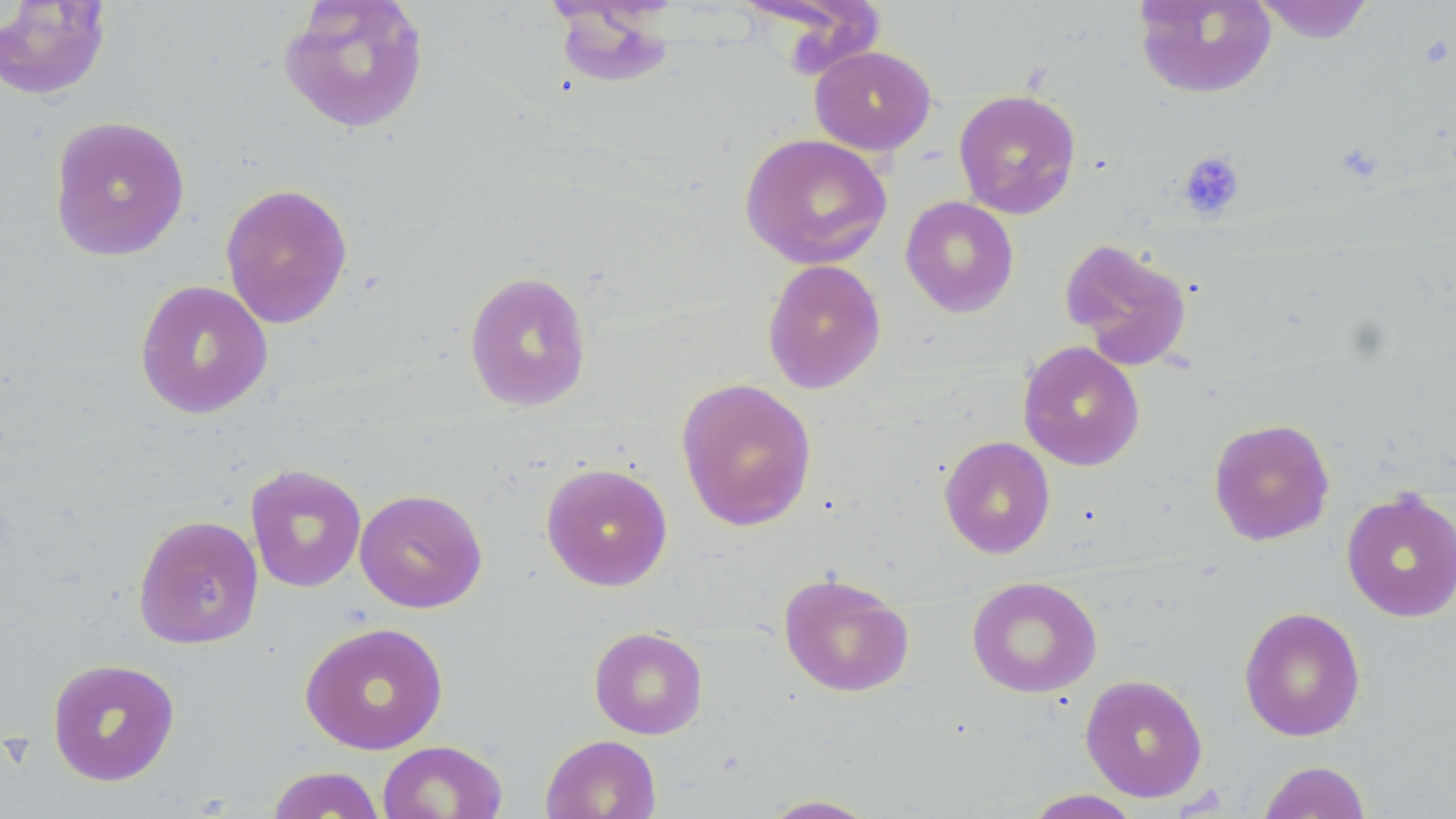

Approximate bounding boxes as (x1, y1, x2, y2) in pixels. Uninfected red blood cell locations: (277, 0, 430, 135), (1133, 0, 1277, 99), (1252, 0, 1376, 44), (0, 1, 112, 100), (549, 1, 676, 90), (810, 45, 937, 155), (953, 88, 1081, 219), (48, 115, 191, 262), (740, 133, 892, 270), (220, 182, 353, 329), (900, 196, 1020, 317), (1060, 238, 1194, 371), (762, 259, 887, 394), (463, 271, 592, 411), (134, 279, 273, 419), (1017, 341, 1145, 471), (675, 377, 817, 531), (1208, 417, 1335, 546), (939, 435, 1056, 558), (540, 462, 673, 591), (244, 463, 367, 593), (354, 488, 488, 614), (1340, 488, 1456, 623), (132, 513, 264, 650), (778, 571, 914, 698), (966, 576, 1103, 699), (1238, 606, 1367, 742), (299, 621, 448, 755), (589, 626, 708, 739), (46, 657, 181, 786), (1080, 674, 1208, 802), (541, 733, 661, 819), (377, 740, 508, 819), (1257, 760, 1373, 818), (266, 765, 386, 818), (1022, 789, 1144, 818), (759, 794, 881, 818). Platelet locations: (1179, 150, 1246, 221). Slide-level diagnosis: negative for blood parasites. May-Grünwald-Giemsa-stained preparation. Image is 1456×819 pixels. Thin blood smear. Captured at 1000x magnification. Optical microscopy. Single field of view.